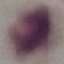 Malaria status: uninfected. Cell patch, automatically extracted from a larger field of view and resized to 64 × 64 pixels. Acquired by smartphone through the microscope eyepiece. Giemsa-stained preparation. Thin blood film.